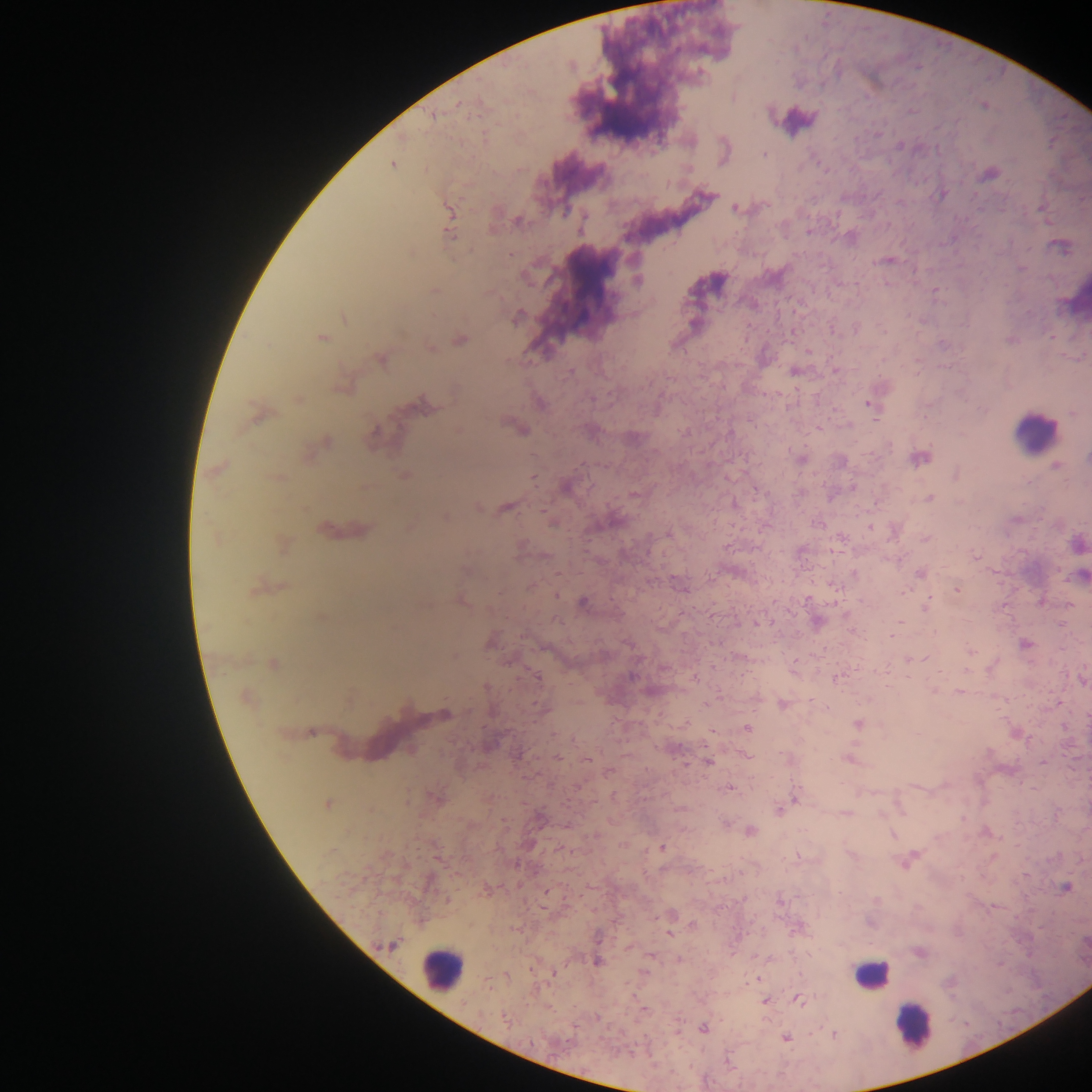 Approximate centers as (x, y) in pixels. Leukocyte locations: (797, 120), (1074, 299), (1035, 431), (442, 969), (871, 976), (912, 1026). Plasmodium parasite locations: (432, 115), (723, 148), (764, 153), (393, 163), (989, 174), (941, 194), (707, 196), (735, 208), (1043, 208), (449, 213), (518, 221), (448, 223), (450, 233), (1060, 244), (888, 260), (1021, 268), (637, 280), (434, 290), (936, 290), (344, 317), (516, 317), (321, 337), (459, 339), (429, 347), (808, 351), (381, 358), (794, 371), (835, 371), (342, 386), (297, 399), (872, 403), (423, 405), (258, 414), (520, 428), (322, 443), (800, 458), (919, 458), (840, 460), (1055, 465), (218, 469), (958, 474), (404, 475), (566, 486), (633, 494), (929, 497), (478, 506), (505, 507), (446, 516), (552, 522), (409, 525), (870, 527), (324, 529), (340, 530), (894, 531), (926, 537), (1078, 543), (282, 544), (975, 555), (920, 572), (1081, 575), (681, 586), (255, 589), (956, 589), (461, 598), (1040, 601), (582, 603), (926, 605), (817, 621), (757, 623), (852, 631), (490, 641), (1024, 643), (970, 651), (909, 658), (273, 664), (836, 677), (694, 678), (1082, 678), (935, 690), (959, 692), (245, 698), (782, 703), (1059, 703), (445, 714), (857, 724), (746, 728), (1016, 732), (745, 754), (558, 758), (787, 758), (848, 758), (587, 759), (708, 761), (1043, 761), (729, 787), (795, 796), (436, 798), (327, 803), (780, 808), (845, 812), (1055, 814), (726, 823), (749, 830), (661, 847), (908, 858), (1065, 888), (486, 889), (546, 892), (668, 923), (670, 933), (390, 944), (919, 951), (679, 960), (597, 961), (758, 979), (797, 999), (764, 1001), (703, 1028), (834, 1033), (786, 1038). One field of view. Collected in Ghana. Mobile-phone photograph taken through the microscope. Thick blood smear. Image is 1092×1092 pixels.